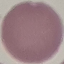

result: negative for malaria parasites
image_type: automatically extracted cell patch, resized to 64 × 64 pixels
stain: Giemsa
capture: smartphone through the microscope eyepiece
preparation: thin smear